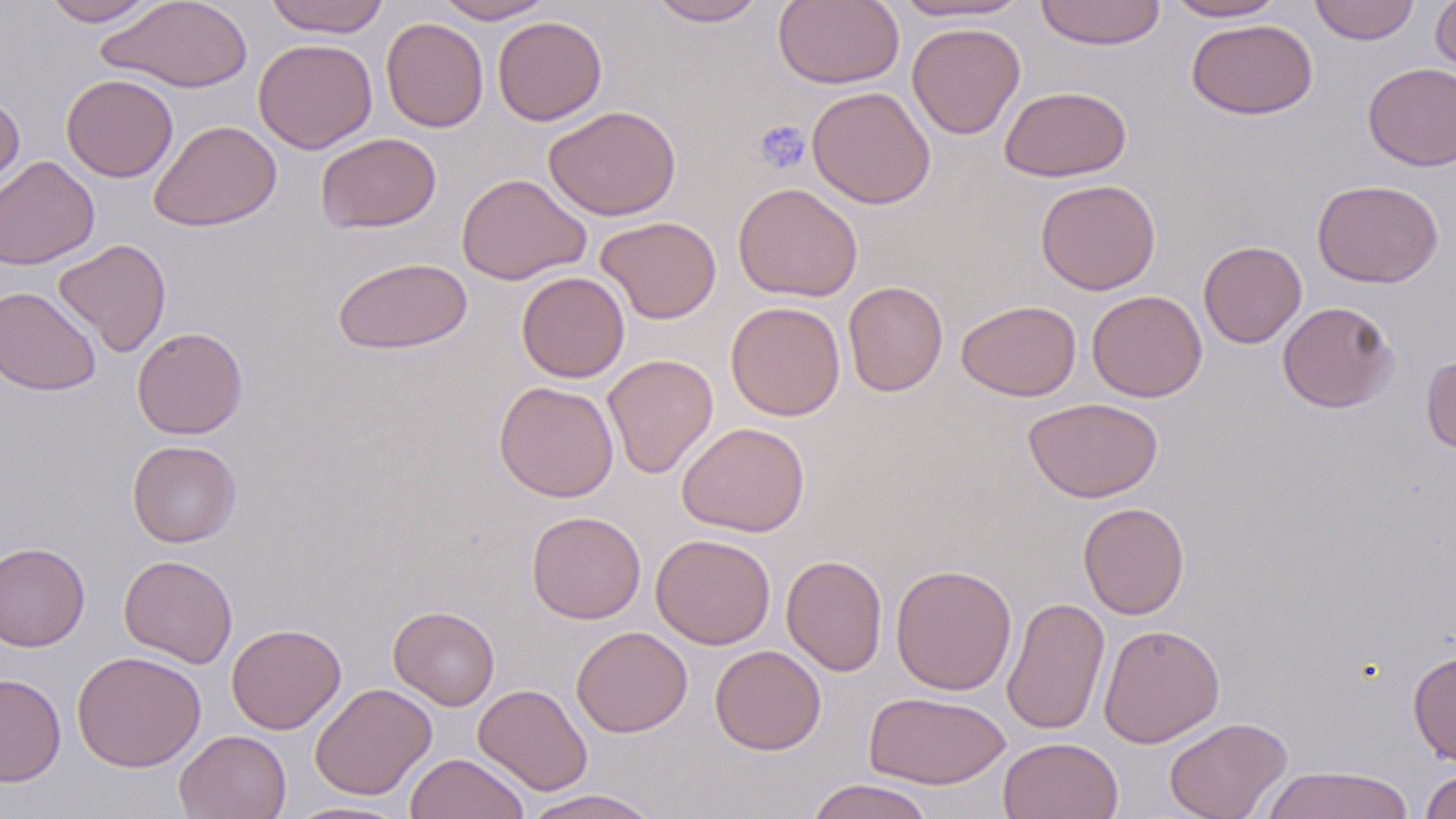

Approximate bounding boxes as (x1,y1)-(x2,y2) corner pairs in pixels. Platelet locations: (753,119)-(811,175). Uninfected red blood cell locations: (40,0)-(158,26), (96,0)-(254,93), (263,0)-(390,37), (434,0)-(555,23), (648,0)-(768,26), (773,0)-(904,89), (891,0)-(1031,22), (1034,0)-(1167,50), (1164,0)-(1287,21), (1309,0)-(1419,45), (1431,0)-(1456,80), (492,16)-(607,125), (381,17)-(489,132), (1186,18)-(1318,120), (907,22)-(1025,140), (253,38)-(377,154), (1362,62)-(1456,170), (61,74)-(178,182), (999,85)-(1132,182), (807,86)-(936,209), (0,91)-(25,201), (542,104)-(682,221), (149,120)-(282,232), (315,132)-(441,233), (0,155)-(100,270), (456,173)-(592,285), (1035,178)-(1161,295), (1312,179)-(1444,288), (732,182)-(863,302), (595,216)-(722,324), (53,238)-(171,357), (1199,240)-(1307,348), (332,257)-(473,355), (516,271)-(630,383), (843,281)-(948,397), (0,286)-(101,396), (1086,289)-(1208,402), (956,299)-(1081,401), (1277,300)-(1400,412), (725,301)-(846,421), (132,327)-(248,439), (1421,352)-(1456,454), (602,353)-(718,479), (494,380)-(619,502), (1023,397)-(1163,503), (676,421)-(810,537), (127,440)-(241,547), (1078,502)-(1189,619), (526,510)-(646,624), (651,533)-(776,649), (0,541)-(90,651), (119,554)-(238,669), (781,554)-(887,676), (890,563)-(1017,695), (1001,596)-(1110,735), (389,605)-(500,710), (226,623)-(346,734), (1098,624)-(1225,747), (571,626)-(693,737), (710,644)-(826,755), (71,650)-(207,772), (1408,650)-(1456,766), (0,673)-(66,786), (310,683)-(436,800), (473,684)-(593,795), (863,691)-(1011,789), (1164,717)-(1292,819), (174,729)-(291,819), (997,736)-(1124,819), (405,753)-(530,819), (1260,765)-(1416,819), (1420,769)-(1456,819), (805,778)-(936,819), (516,789)-(661,819), (283,800)-(415,818). Slide-level diagnosis: no evidence of blood parasites. May-Grünwald-Giemsa-stained preparation. Thin blood film. One field of a larger specimen. 1000x magnification. Image is 1456×819 pixels. Optical microscopy.